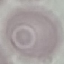
Summary:
  - Result: no malaria parasites seen
  - Preparation: thin blood film
  - Stain: Giemsa
  - Image type: cell patch, automatically extracted from a larger field of view and resized to 64 × 64 pixels
  - Capture: smartphone through the microscope eyepiece